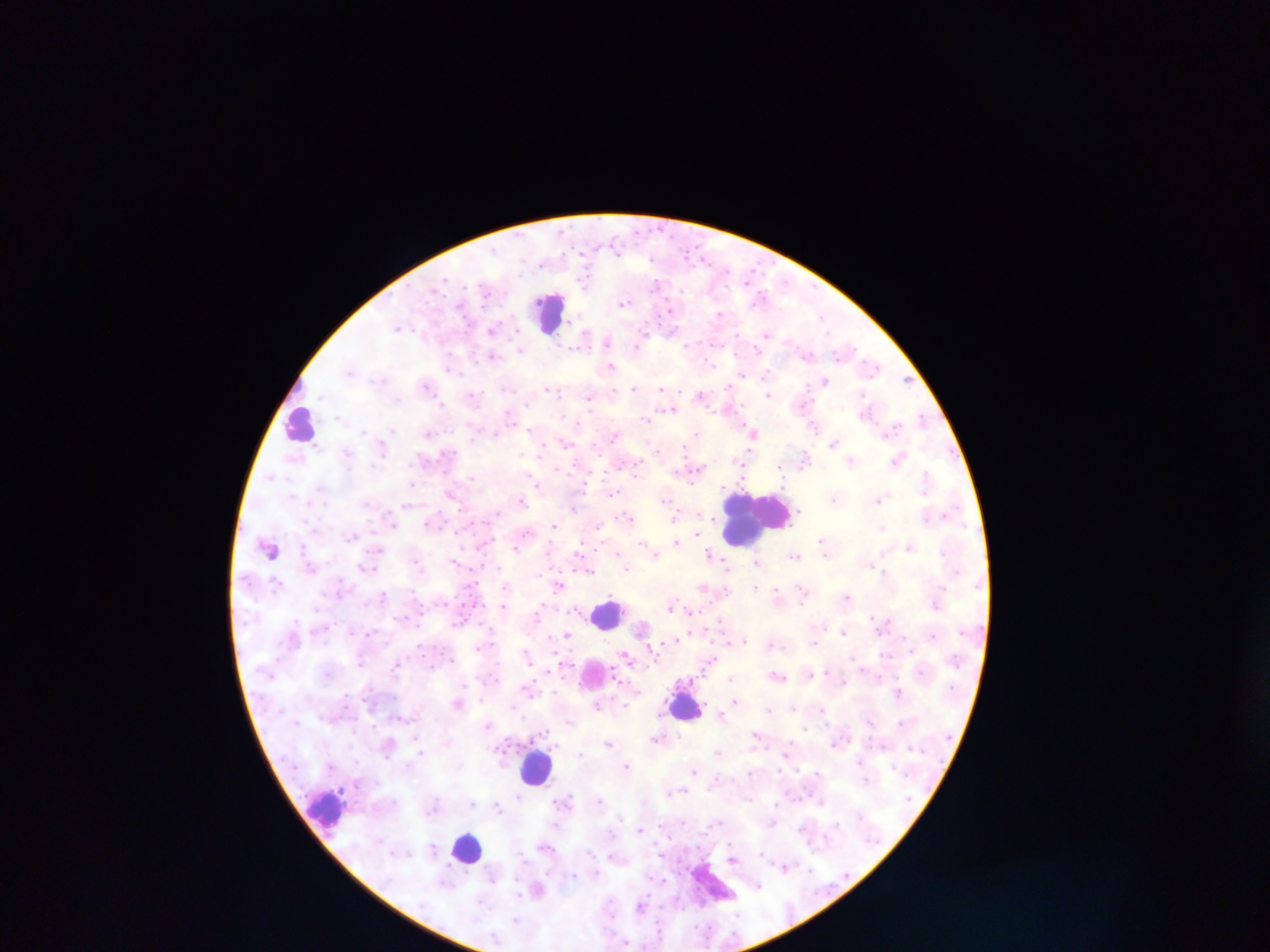

image_size: 1270×952 pixels
plasmodium_parasite_locations: 'approximate centers as {x, y} in pixels: {624, 302}, {671, 311}, {719, 314}, {399, 326}, {492, 328}, {767, 334}, {643, 335}, {608, 341}, {641, 341}, {522, 349}, {492, 355}, {872, 364}, {451, 365}, {611, 366}, {350, 370}, {742, 375}, {906, 379}, {824, 381}, {426, 384}, {635, 387}, {663, 389}, {555, 391}, {768, 394}, {473, 395}, {703, 395}, {591, 396}, {672, 408}, {866, 411}, {922, 417}, {530, 430}, {753, 431}, {429, 432}, {696, 433}, {614, 435}, {567, 443}, {833, 443}, {543, 447}, {898, 458}, {851, 460}, {740, 462}, {781, 467}, {928, 478}, {412, 484}, {538, 485}, {614, 491}, {451, 494}, {835, 499}, {665, 500}, {879, 500}, {521, 501}, {574, 507}, {677, 515}, {626, 517}, {927, 517}, {394, 523}, {553, 526}, {882, 527}, {698, 535}, {677, 541}, {824, 542}, {910, 546}, {515, 547}, {580, 552}, {618, 552}, {655, 554}, {710, 554}, {796, 555}, {455, 561}, {758, 561}, {727, 564}, {366, 566}, {560, 584}, {505, 586}, {757, 586}, {704, 587}, {777, 592}, {803, 593}, {846, 596}, {504, 606}, {671, 606}, {690, 611}, {539, 612}, {844, 631}, {370, 633}, {567, 635}, {933, 635}, {678, 640}, {743, 640}, {814, 642}, {773, 644}, {649, 646}, {526, 653}, {625, 656}, {712, 659}, {361, 660}, {563, 663}, {398, 664}, {548, 671}, {829, 671}, {810, 673}, {777, 675}, {879, 676}, {731, 679}, {620, 682}, {843, 682}, {528, 688}, {899, 693}, {735, 700}, {459, 702}, {599, 704}, {769, 709}, {822, 709}, {488, 724}, {757, 734}, {656, 738}, {836, 741}, {609, 742}, {389, 744}, {719, 751}, {421, 753}, {787, 753}, {581, 755}, {860, 761}, {626, 765}, {694, 770}, {750, 772}, {600, 801}, {564, 802}, {821, 802}, {472, 804}, {497, 807}, {663, 826}, {641, 828}, {546, 847}, {733, 858}, {784, 867}, {494, 877}, {757, 885}, {537, 888}, {641, 906}'
capture: mobile-phone photograph through a microscope
preparation: thick blood smear
field_of_view: single
leukocyte_locations: 'approximate centers as {x, y} in pixels: {551, 312}, {300, 423}, {755, 517}, {270, 548}, {607, 613}, {596, 677}, {685, 705}, {536, 767}, {327, 809}, {467, 848}'
country: Ghana